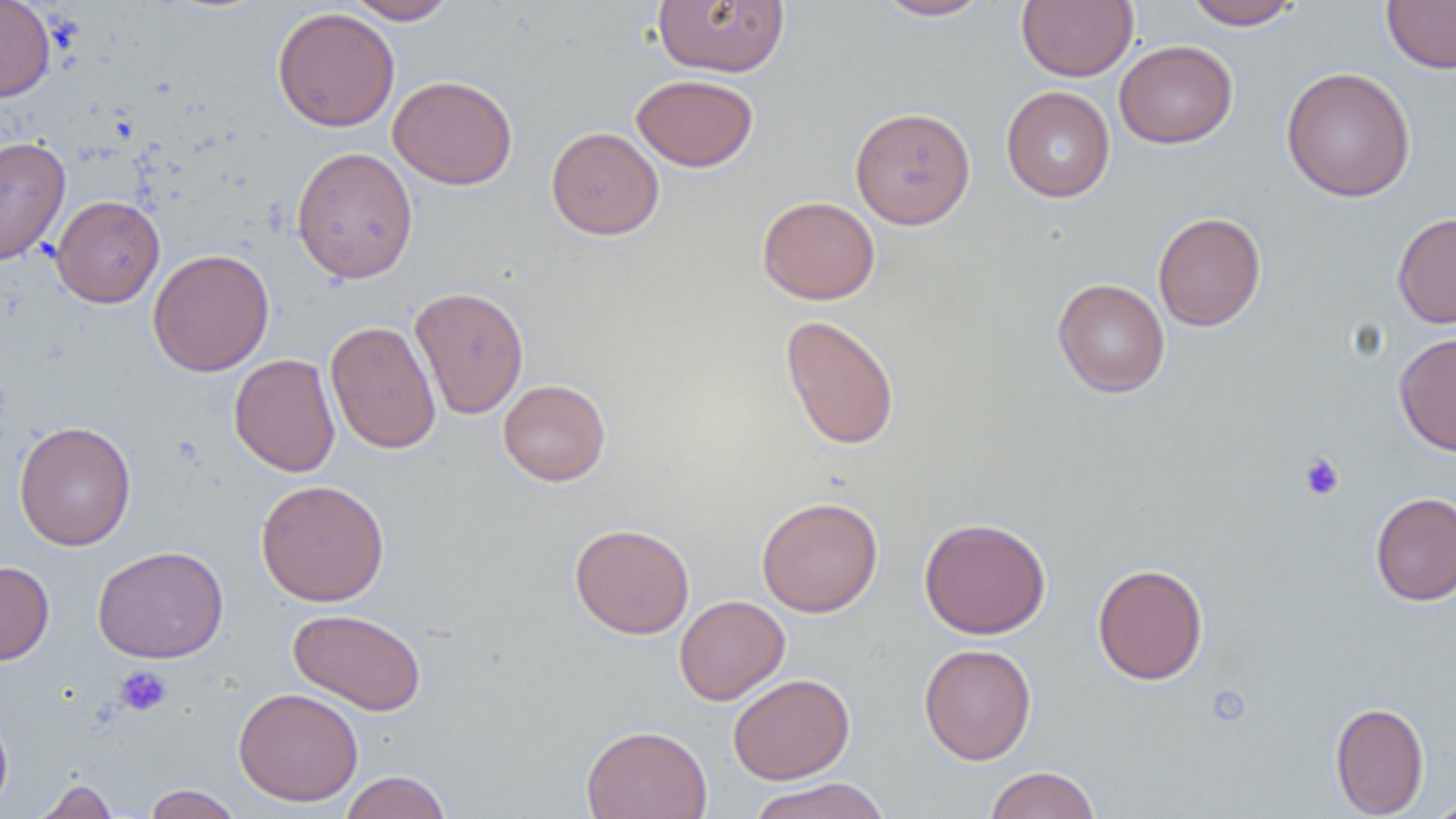
{
  "slide_level_diagnosis": "negative for blood parasites",
  "magnification": "1000x",
  "image_size": "1456×819 pixels",
  "platelet_locations": "approximate bounding boxes as (x1, y1, x2, y2) in pixels: (1299, 453, 1345, 501), (115, 666, 172, 716)",
  "uninfected_red_blood_cell_locations": "approximate bounding boxes as (x1, y1, x2, y2) in pixels: (0, 0, 56, 102), (344, 0, 457, 24), (653, 0, 790, 76), (874, 0, 992, 20), (1017, 0, 1138, 81), (1184, 0, 1301, 30), (1382, 1, 1456, 73), (272, 6, 400, 132), (1114, 39, 1238, 148), (1281, 66, 1416, 202), (631, 74, 758, 172), (388, 75, 518, 190), (1001, 86, 1115, 202), (850, 106, 976, 230), (546, 126, 664, 240), (0, 135, 71, 266), (291, 146, 418, 284), (51, 194, 165, 308), (757, 195, 880, 304), (1153, 212, 1266, 332), (1392, 212, 1456, 328), (147, 248, 275, 376), (1052, 278, 1170, 398), (410, 286, 529, 420), (780, 314, 900, 450), (325, 320, 442, 454), (1394, 331, 1456, 455), (228, 353, 340, 477), (498, 379, 611, 486), (14, 420, 136, 551), (256, 479, 390, 606), (1370, 492, 1456, 606), (757, 496, 883, 617), (919, 517, 1051, 639), (569, 522, 695, 639), (92, 545, 229, 663), (0, 561, 55, 664), (1092, 562, 1208, 685), (674, 595, 790, 705), (288, 608, 427, 715), (918, 643, 1036, 764), (728, 673, 855, 784), (233, 687, 364, 806), (1330, 701, 1430, 818), (0, 711, 13, 815), (581, 724, 712, 819), (983, 765, 1101, 819), (339, 770, 451, 819), (747, 777, 893, 819), (33, 778, 119, 818), (142, 784, 244, 819), (1424, 796, 1456, 819)",
  "modality": "optical microscopy",
  "preparation": "thin blood smear",
  "field_of_view": "one of a larger specimen"
}